Report the malaria status of this cell.
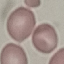

It is uninfected.

Giemsa-stained preparation. Thin blood smear. Cell patch, automatically extracted from a larger field of view and resized to 64 × 64 pixels. Photographed with a smartphone camera at the microscope eyepiece.